Outline each Plasmodium falciparum-infected red blood cell.
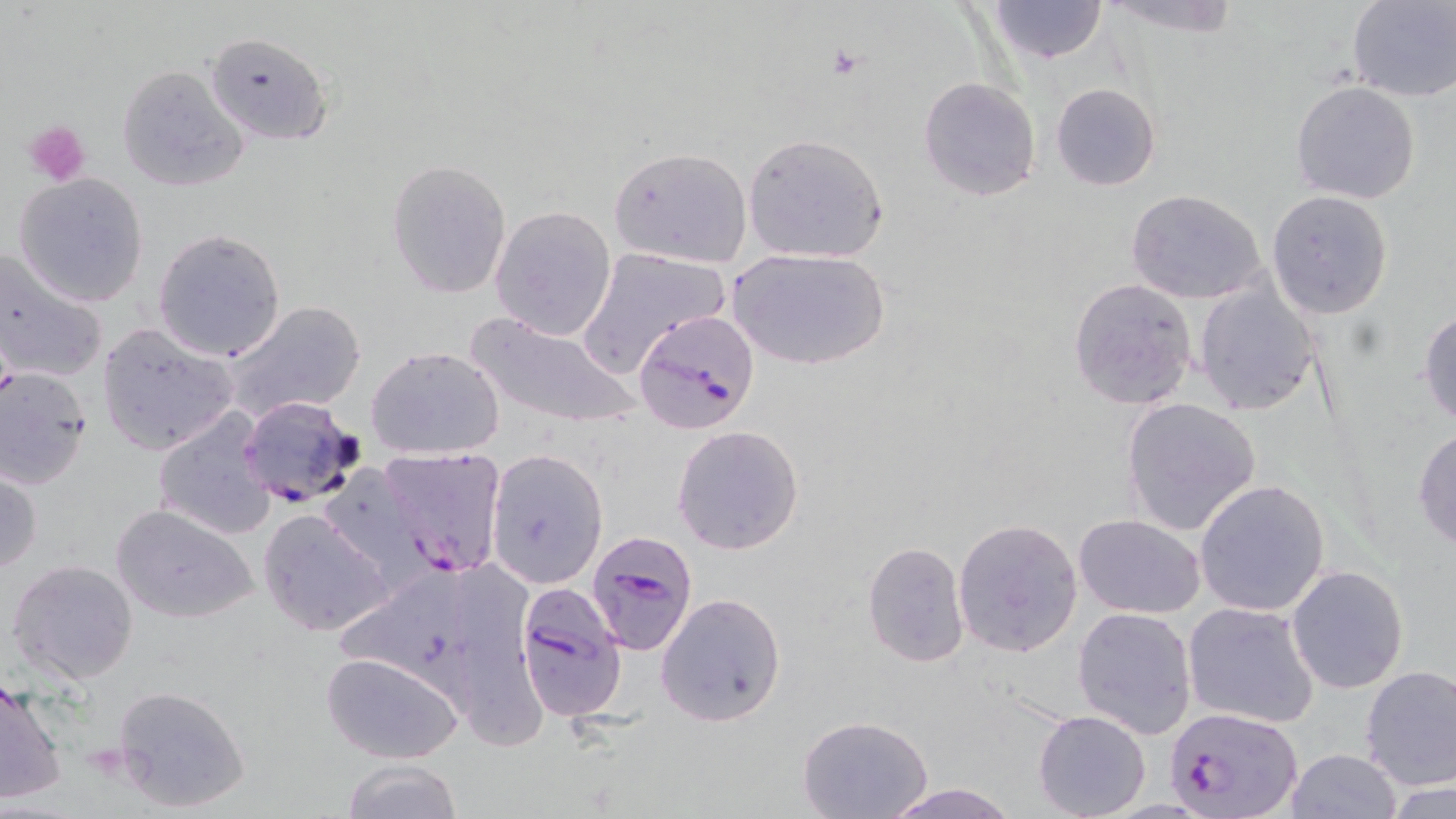

Approximate bounding boxes as (x1, y1, x2, y2) in pixels.
Plasmodium falciparum-infected red blood cells: (633, 307, 761, 435), (335, 468, 468, 602), (585, 529, 701, 654), (512, 587, 628, 725), (1165, 704, 1302, 818).

Summary:
  - Uninfected red blood cell locations: (987, 0, 1110, 64), (1094, 0, 1244, 38), (1345, 0, 1455, 101), (204, 31, 333, 148), (116, 64, 249, 192), (917, 77, 1042, 202), (1290, 81, 1420, 204), (1050, 83, 1161, 192), (742, 132, 890, 265), (608, 146, 752, 269), (386, 159, 512, 300), (14, 172, 148, 307), (1125, 189, 1268, 306), (1266, 190, 1396, 320), (490, 204, 616, 340), (153, 228, 287, 362), (577, 246, 732, 377), (730, 247, 888, 371), (0, 249, 107, 387), (1068, 277, 1198, 410), (1195, 281, 1323, 416), (220, 300, 368, 427), (1418, 309, 1456, 426), (464, 310, 642, 429), (97, 322, 239, 456), (364, 346, 506, 463), (0, 367, 94, 490), (239, 394, 365, 509), (1120, 397, 1261, 537), (152, 406, 277, 539), (671, 424, 804, 556), (1412, 426, 1456, 552), (378, 447, 510, 555), (485, 449, 609, 590), (1, 466, 43, 577), (1194, 479, 1332, 617), (110, 503, 260, 624), (258, 510, 394, 637), (1074, 515, 1205, 618), (952, 516, 1084, 658), (862, 541, 971, 667), (7, 560, 138, 685), (1286, 565, 1408, 694), (655, 592, 786, 727), (1182, 601, 1320, 729), (1073, 607, 1197, 739), (321, 650, 464, 764), (1359, 664, 1456, 790), (0, 676, 68, 805), (111, 683, 254, 815), (1031, 710, 1152, 819), (797, 716, 934, 819), (1283, 749, 1401, 819), (339, 759, 464, 819), (1384, 779, 1453, 819), (879, 782, 1022, 819)
  - Platelet locations: (828, 46, 865, 77), (25, 119, 92, 186), (81, 743, 128, 784)
  - Slide-level diagnosis: Plasmodium falciparum
  - Magnification: 1000x
  - Image size: 1456×819 pixels
  - Preparation: thin blood smear
  - Stain: May-Grünwald-Giemsa
  - Field of view: single
  - Modality: light microscopy